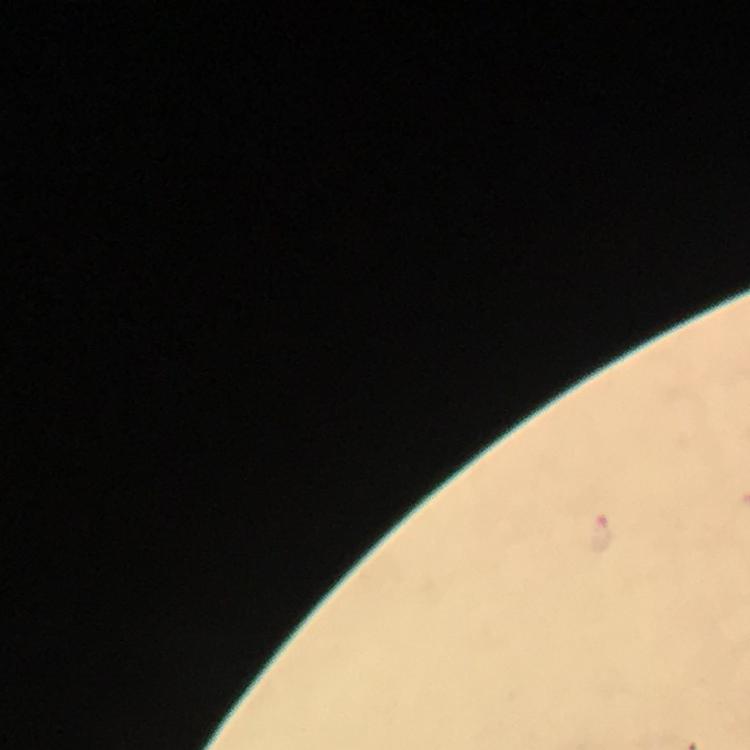
{
  "cropped_from": "one field of view",
  "stain": "Giemsa",
  "immersion_oil": "applied",
  "context": "from a diagnostic examination for malaria",
  "preparation": "thick smear",
  "magnification": "100x",
  "capture": "smartphone mounted on the microscope",
  "plasmodium_parasite_locations": "approximate centers as [x, y] in pixels: [600, 534]",
  "image_size": "750×750 pixels"
}